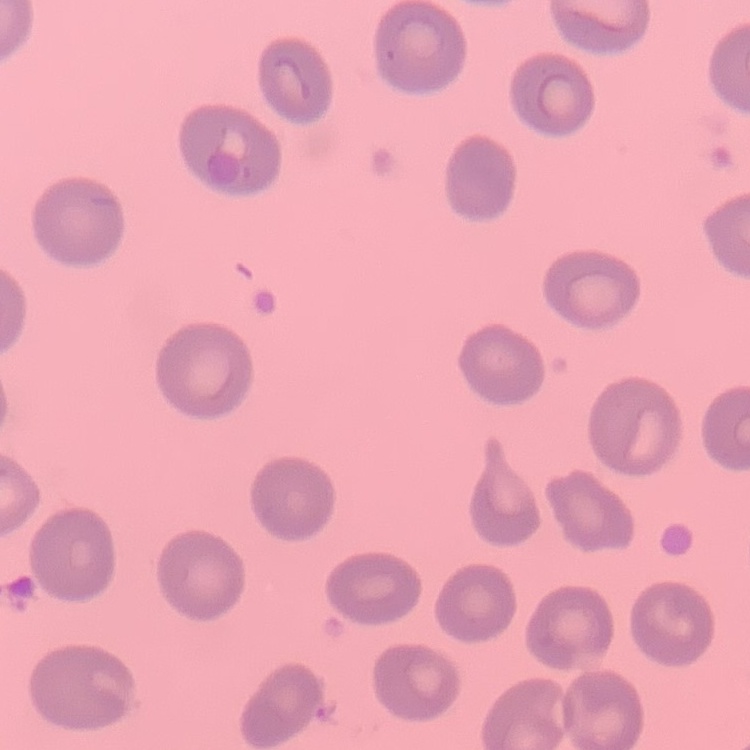
Summary:
  - Red blood cell morphology: no rouleaux formation
  - Preparation: thin peripheral smear
  - Image type: square crop of a larger photomicrograph
  - Stain: Field's or Giemsa